Comment on the morphology of the erythrocytes.
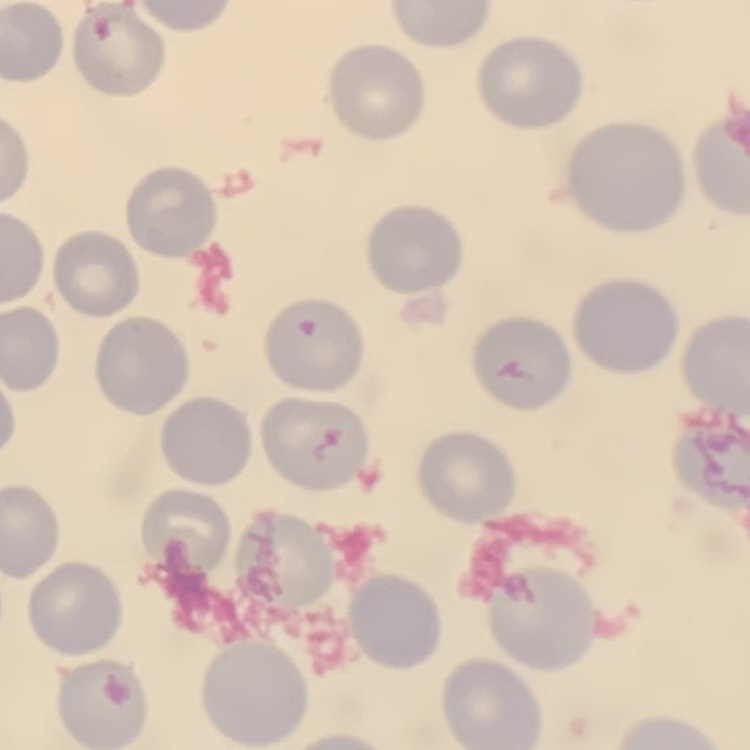

They show no rouleaux formation.

Summary:
  - Stain: Field's or Giemsa
  - Image type: square crop of a larger photomicrograph
  - Preparation: thin blood smear